Describe the morphology of the erythrocytes.
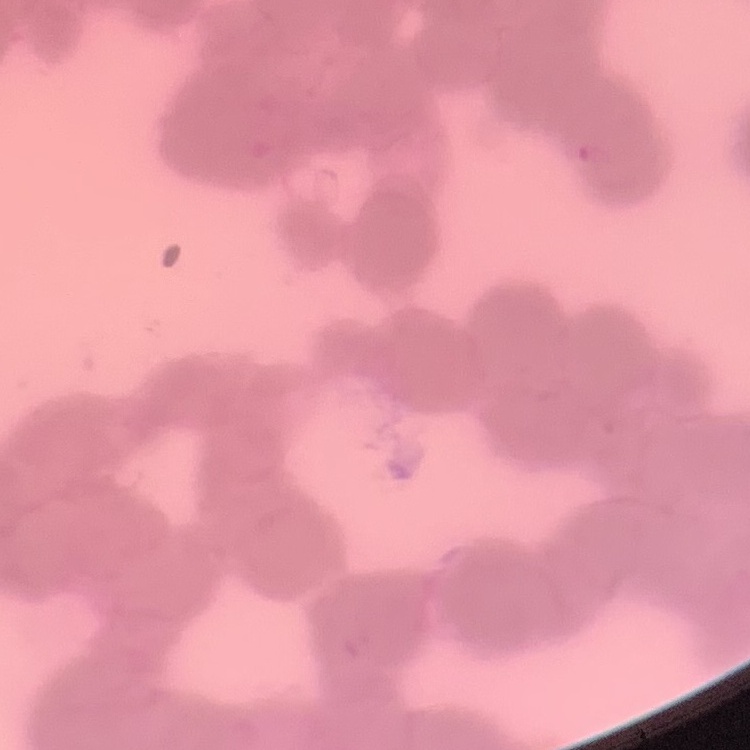

Rouleaux formation.

Summary:
  - Image type: one tile cut from a larger photomicrograph
  - Stain: Field's or Giemsa
  - Preparation: thin blood smear